Locate every blood parasite and identify its species.
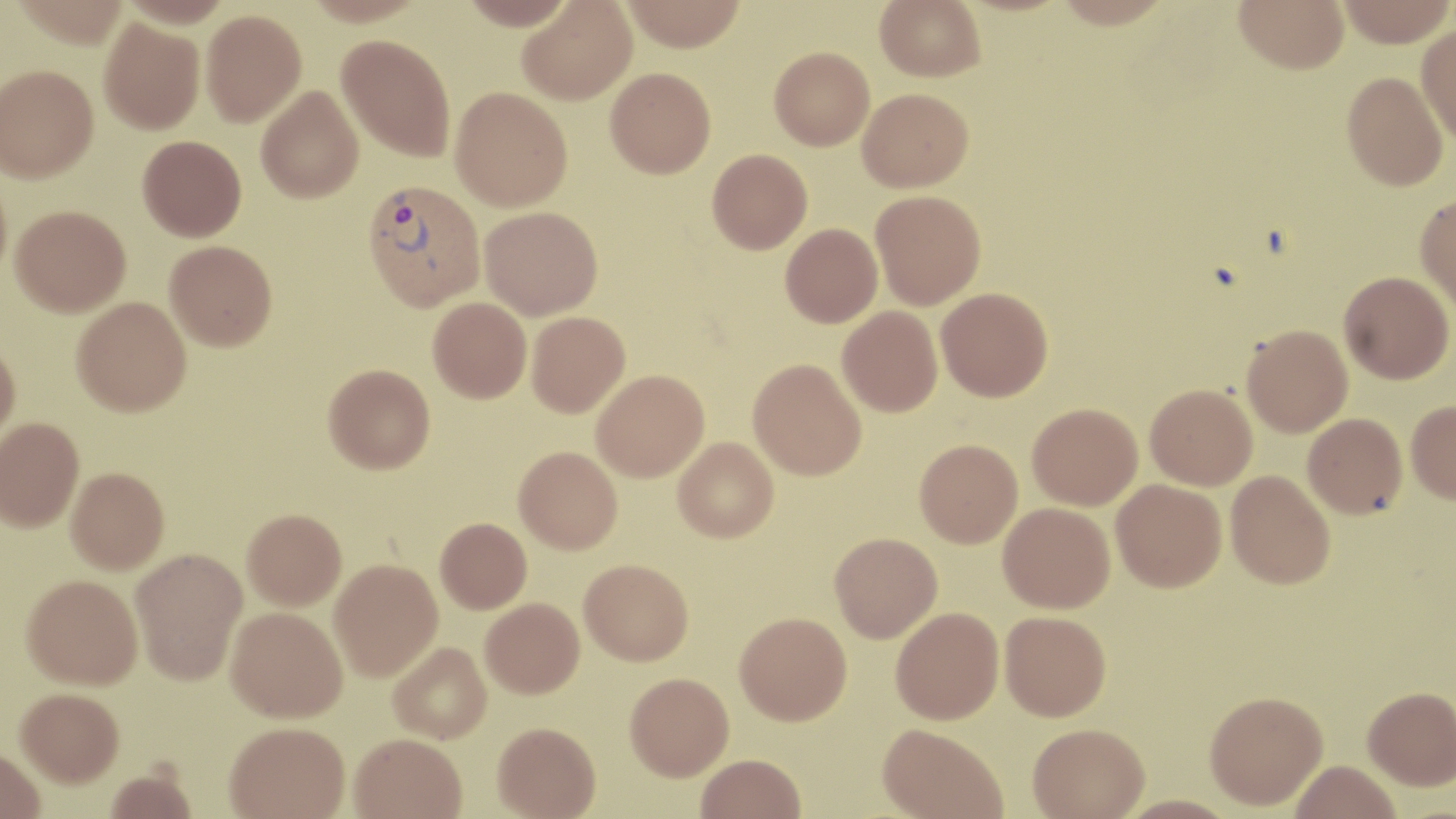
Approximate bounding boxes as (x1,y1)-(x2,y2) corner pairs in pixels.
Plasmodium vivax-infected red blood cells: (361,179)-(485,311).
No Plasmodium falciparum, Plasmodium ovale, Plasmodium malariae, Babesia divergens, or Trypanosoma brucei observed.

slide-level diagnosis = Plasmodium vivax
image size = 1456×819 pixels
field of view = single
uninfected red blood cell locations = approximate bounding boxes as (x1,y1)-(x2,y2) corner pairs in pixels: (303,0)-(427,26), (459,0)-(575,29), (621,0)-(748,52), (875,0)-(986,82), (1234,0)-(1349,73), (1338,0)-(1455,46), (517,1)-(637,105), (201,9)-(306,126), (99,19)-(204,134), (1416,24)-(1456,144), (336,34)-(456,162), (769,46)-(874,150), (0,64)-(98,182), (605,67)-(716,178), (1342,71)-(1449,191), (256,86)-(363,203), (450,86)-(573,211), (857,88)-(973,192), (137,135)-(246,241), (707,149)-(812,254), (0,171)-(12,287), (870,190)-(986,309), (1415,194)-(1456,313), (10,204)-(131,316), (480,206)-(602,319), (781,223)-(883,327), (164,240)-(277,351), (1339,271)-(1454,383), (936,288)-(1053,401), (72,296)-(191,416), (428,297)-(532,403), (837,306)-(943,416), (527,311)-(630,417), (1241,324)-(1353,437), (0,341)-(20,444), (748,358)-(866,480), (324,363)-(435,473), (591,370)-(709,481), (1145,383)-(1257,490), (1406,400)-(1456,504), (1027,403)-(1142,510), (1302,413)-(1407,518), (0,417)-(84,532), (673,437)-(779,542), (915,438)-(1022,547), (514,446)-(622,554), (66,467)-(169,574), (1225,470)-(1335,589), (1111,479)-(1227,592), (998,502)-(1115,613), (242,509)-(346,611), (435,518)-(532,613), (830,532)-(942,641), (130,548)-(247,685), (579,558)-(693,665), (329,559)-(442,681), (21,574)-(143,689), (480,598)-(584,697), (226,606)-(347,722), (891,607)-(1004,724), (1000,610)-(1111,721), (735,612)-(852,725), (389,642)-(491,743), (625,672)-(733,779), (1363,686)-(1456,789), (14,687)-(123,787), (1205,690)-(1328,809), (493,721)-(601,818), (224,722)-(349,819), (1027,722)-(1150,818), (877,723)-(1008,818), (349,733)-(467,819), (0,750)-(45,819), (695,753)-(806,818), (1288,760)-(1402,819), (104,767)-(198,818), (1115,794)-(1240,817)
stain = May-Grünwald-Giemsa
preparation = thin blood smear
magnification = 1000x
modality = optical microscopy